Outline each blood parasite and name the species.
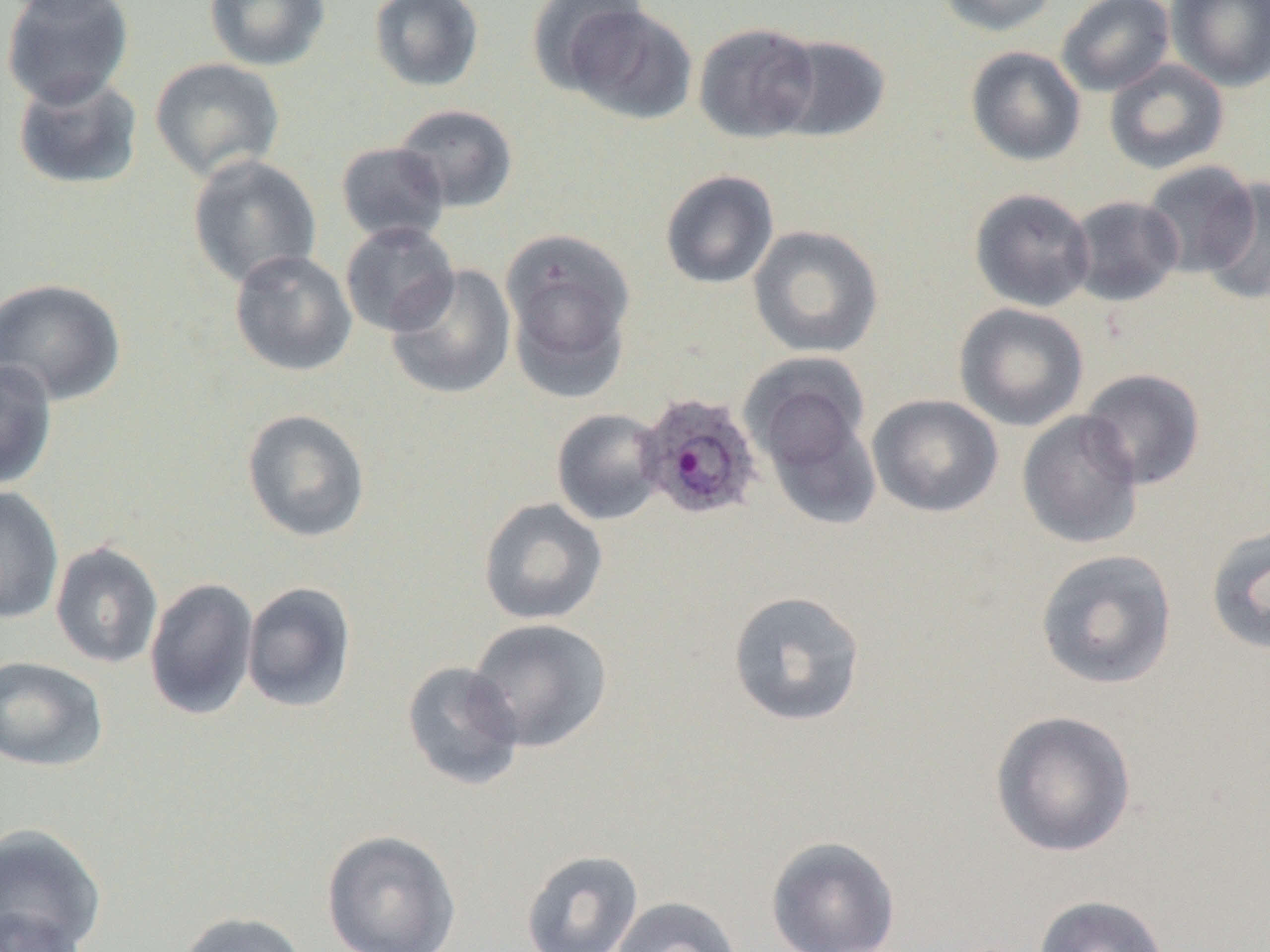

Approximate bounding boxes as named x1/y1/x2/y2 corners in pixels.
Plasmodium ovale-infected red blood cells: (x1=638, y1=392, x2=764, y2=520).
No Plasmodium falciparum, Plasmodium malariae, Plasmodium vivax, Babesia divergens, or Trypanosoma brucei observed.

Uninfected red blood cell locations: (x1=1, y1=0, x2=136, y2=109), (x1=3, y1=0, x2=129, y2=22), (x1=204, y1=0, x2=331, y2=71), (x1=368, y1=0, x2=485, y2=92), (x1=527, y1=0, x2=650, y2=96), (x1=934, y1=0, x2=1060, y2=37), (x1=1056, y1=0, x2=1176, y2=96), (x1=1167, y1=0, x2=1270, y2=92), (x1=561, y1=4, x2=698, y2=126), (x1=693, y1=21, x2=821, y2=143), (x1=771, y1=34, x2=892, y2=143), (x1=965, y1=46, x2=1087, y2=166), (x1=149, y1=57, x2=286, y2=181), (x1=1104, y1=58, x2=1230, y2=175), (x1=12, y1=72, x2=144, y2=191), (x1=393, y1=104, x2=519, y2=213), (x1=335, y1=142, x2=451, y2=244), (x1=187, y1=154, x2=322, y2=289), (x1=1140, y1=161, x2=1260, y2=278), (x1=659, y1=170, x2=779, y2=290), (x1=1198, y1=178, x2=1270, y2=303), (x1=969, y1=188, x2=1095, y2=312), (x1=1067, y1=195, x2=1184, y2=306), (x1=339, y1=220, x2=460, y2=337), (x1=748, y1=225, x2=884, y2=358), (x1=501, y1=229, x2=637, y2=396), (x1=229, y1=249, x2=358, y2=377), (x1=386, y1=264, x2=516, y2=400), (x1=0, y1=277, x2=127, y2=406), (x1=954, y1=303, x2=1089, y2=432), (x1=0, y1=358, x2=58, y2=490), (x1=746, y1=363, x2=880, y2=526), (x1=1079, y1=368, x2=1206, y2=490), (x1=867, y1=394, x2=1003, y2=518), (x1=241, y1=408, x2=371, y2=543), (x1=551, y1=408, x2=667, y2=526), (x1=1017, y1=410, x2=1144, y2=549), (x1=0, y1=485, x2=64, y2=624), (x1=478, y1=497, x2=608, y2=626), (x1=1205, y1=521, x2=1270, y2=657), (x1=50, y1=542, x2=163, y2=668), (x1=1035, y1=548, x2=1178, y2=690), (x1=144, y1=577, x2=259, y2=721), (x1=241, y1=582, x2=356, y2=713), (x1=728, y1=590, x2=866, y2=727), (x1=466, y1=618, x2=613, y2=753), (x1=0, y1=655, x2=109, y2=772), (x1=400, y1=661, x2=525, y2=791), (x1=989, y1=708, x2=1137, y2=858), (x1=0, y1=822, x2=107, y2=952), (x1=321, y1=829, x2=462, y2=952), (x1=765, y1=835, x2=901, y2=952), (x1=520, y1=849, x2=643, y2=952), (x1=1032, y1=894, x2=1171, y2=952), (x1=609, y1=896, x2=742, y2=952), (x1=0, y1=903, x2=89, y2=952), (x1=175, y1=911, x2=310, y2=952). Slide-level diagnosis: Plasmodium ovale. 1000x magnification. Thin blood film. One field of a larger specimen. Optical microscopy. Image is 1270×952 pixels.